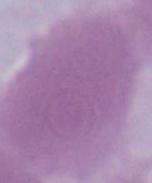

{
  "modality": "photomicrograph",
  "identification": "erythrocyte",
  "magnification": "1000x"
}